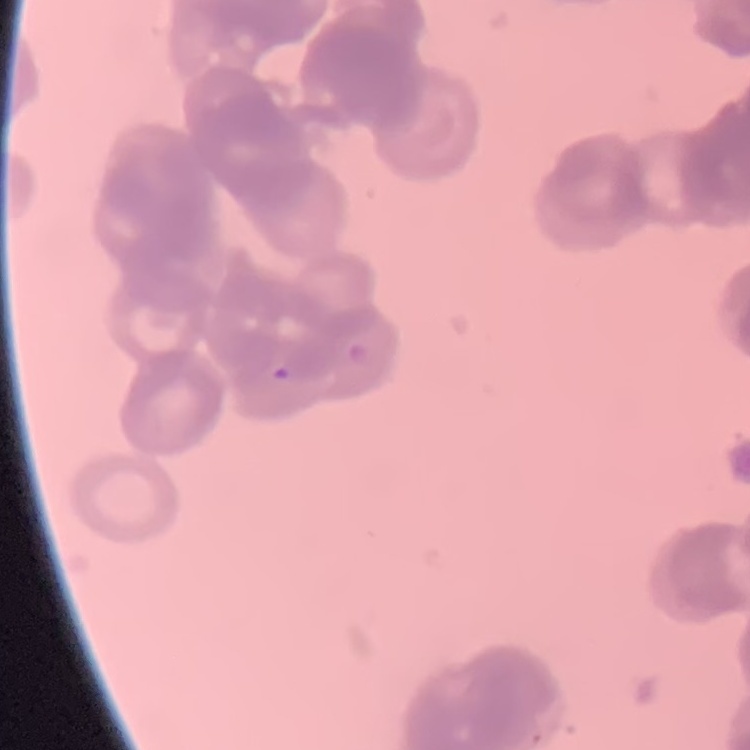
red blood cell morphology = rouleaux formation
preparation = thin peripheral smear
stain = Field's or Giemsa
image type = one tile cut from a larger photomicrograph